Classify this cell by malaria status.
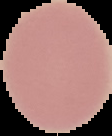

Uninfected.

Image is 112×136 pixels. Segmented cell region on a black background. From a thin blood smear.